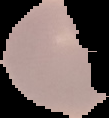

image_type: segmented cell region with the area outside set to black
image_size: 109×118 pixels
result: negative for malaria parasites
preparation: thin blood smear